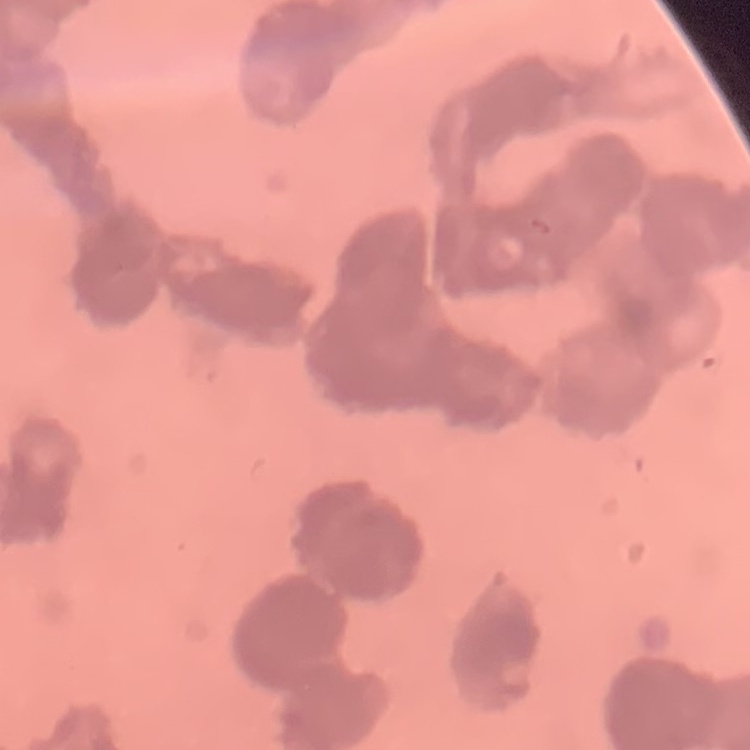

erythrocyte_morphology: rouleaux formation
image_type: one tile cut from a larger photomicrograph
preparation: thin blood film
stain: Field's or Giemsa